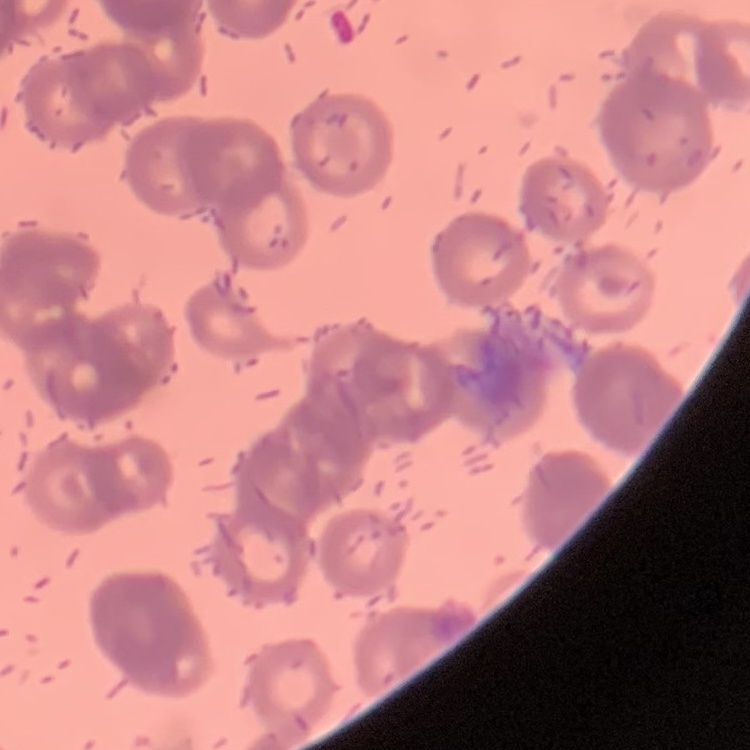

Summary:
  - Red blood cell morphology: rouleaux formation
  - Stain: Field's or Giemsa
  - Image type: one tile cut from a larger photomicrograph
  - Preparation: thin blood smear